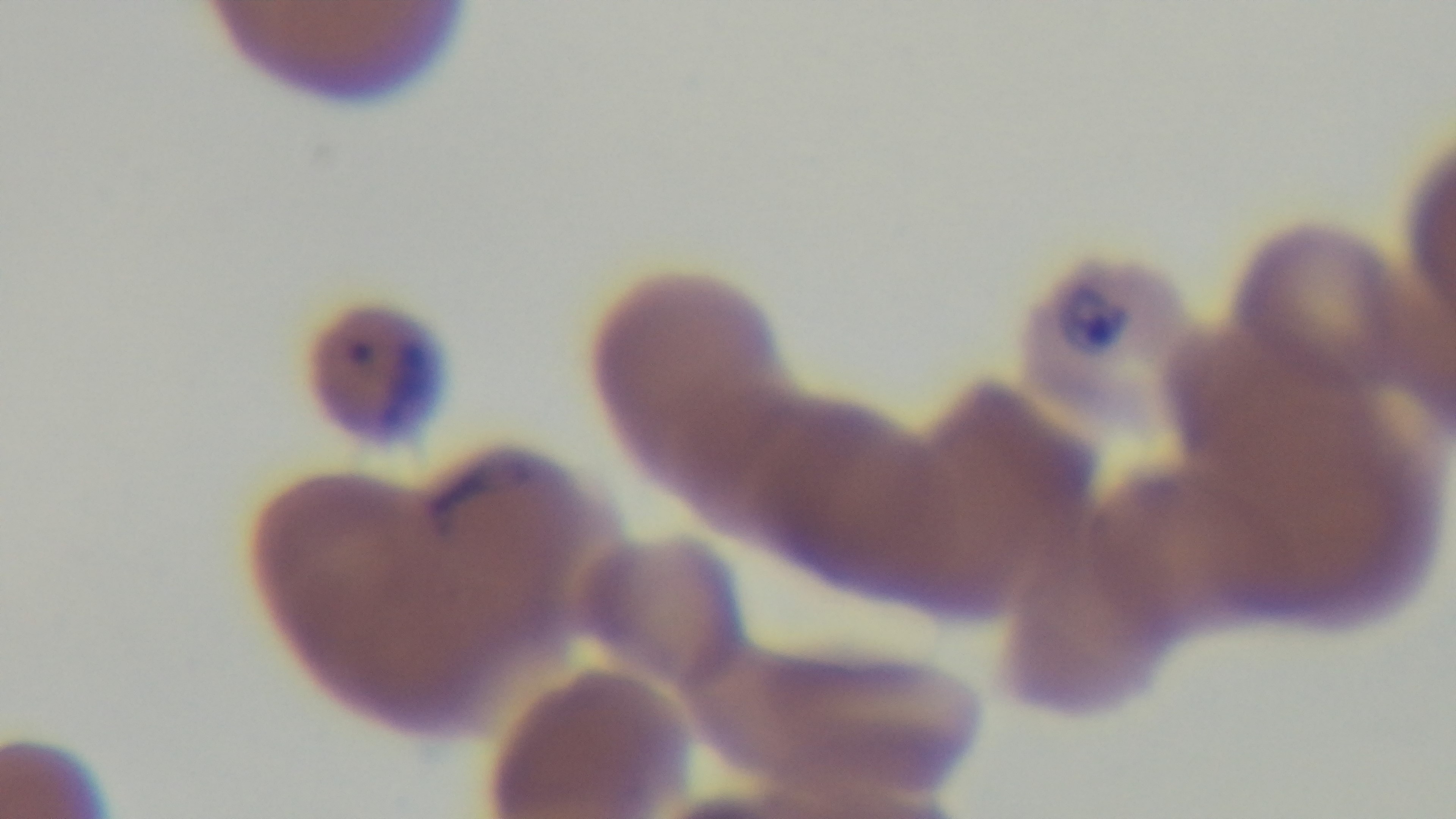 Photomicrograph. Malaria status: positive. Oil-immersion objective, 100x. Captured with a mounted 4K digital camera. Giemsa-stained. Preparation: thin smear. One field from the slide.